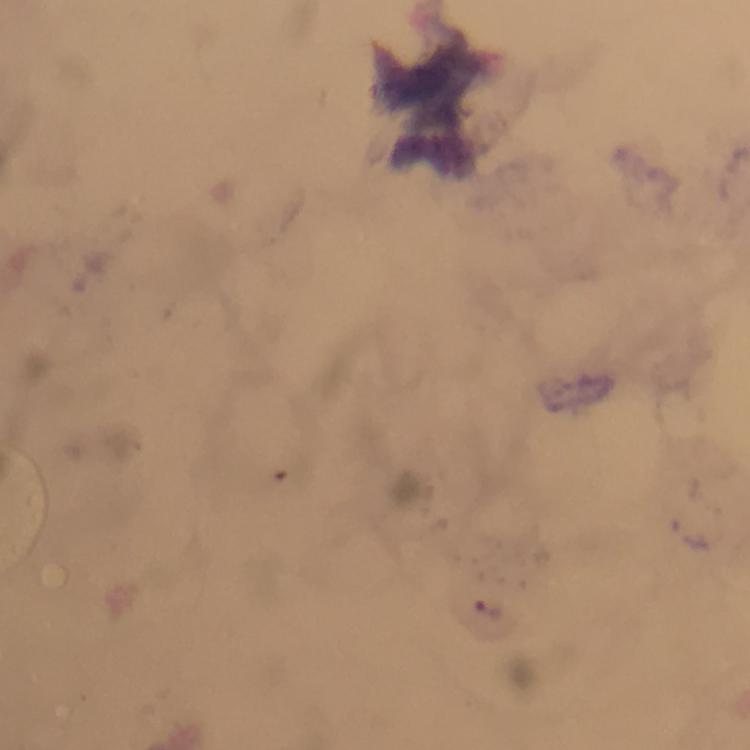
capture = smartphone photograph through a microscope
preparation = thick blood smear
stain = Giemsa
cropped from = a single field of view
image size = 750×750 pixels
magnification = 100x
malaria parasite locations = approximate centers as [x, y] in pixels: [489, 611]
immersion oil = applied
context = from a diagnostic examination for malaria